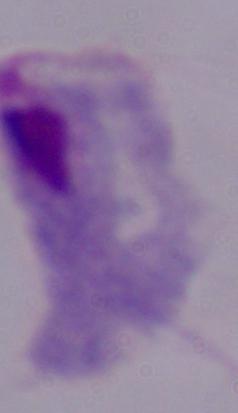

Summary:
  - Magnification: 1000x
  - Identification: trichomonad
  - Modality: photomicrograph